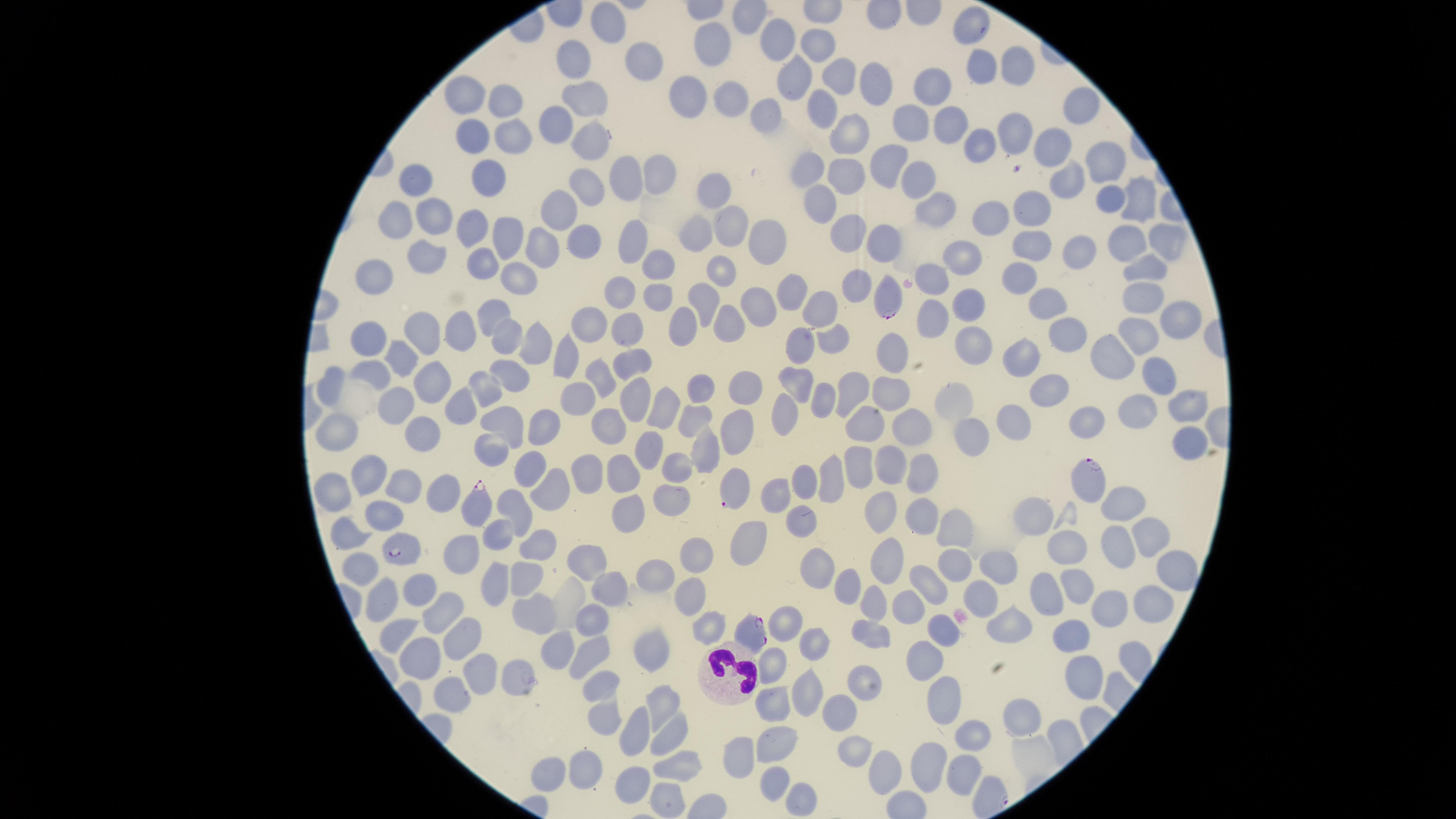 Approximate marker points as {x, y} in pixels. White blood cells: {721, 674}. Uninfected red blood cells: {605, 18}, {975, 27}, {782, 36}, {714, 42}, {818, 47}, {645, 57}, {568, 60}, {981, 65}, {1018, 66}, {796, 78}, {844, 78}, {873, 80}, {933, 87}, {691, 90}, {466, 95}, {586, 96}, {502, 100}, {734, 101}, {824, 106}, {1079, 113}, {764, 117}, {913, 120}, {556, 121}, {944, 125}, {1009, 133}, {469, 134}, {507, 137}, {850, 137}, {590, 139}, {973, 146}, {1049, 150}, {1102, 164}, {892, 166}, {665, 168}, {808, 168}, {629, 170}, {844, 172}, {485, 181}, {916, 181}, {589, 184}, {418, 185}, {1062, 185}, {708, 192}, {1133, 199}, {1110, 202}, {824, 204}, {927, 209}, {556, 212}, {1037, 212}, {436, 215}, {999, 216}, {397, 221}, {734, 224}, {475, 230}, {771, 233}, {1169, 233}, {502, 236}, {845, 236}, {583, 239}, {887, 239}, {692, 240}, {1123, 240}, {637, 241}, {1033, 246}, {538, 248}, {1079, 248}, {429, 255}, {963, 255}, {484, 260}, {664, 263}, {1145, 268}, {716, 272}, {378, 275}, {1018, 276}, {933, 279}, {518, 280}, {859, 282}, {617, 289}, {785, 289}, {704, 296}, {654, 297}, {760, 297}, {1141, 300}, {969, 301}, {1048, 304}, {825, 306}, {933, 312}, {492, 317}, {1176, 318}, {623, 324}, {589, 325}, {684, 329}, {732, 330}, {461, 332}, {370, 334}, {1141, 336}, {428, 337}, {1064, 338}, {505, 339}, {838, 339}, {533, 341}, {804, 346}, {980, 347}, {896, 348}, {564, 353}, {1111, 353}, {1029, 356}, {399, 357}, {626, 362}, {370, 369}, {1154, 369}, {507, 378}, {598, 380}, {332, 381}, {433, 382}, {701, 383}, {801, 383}, {740, 386}, {895, 387}, {1047, 387}, {852, 388}, {483, 394}, {825, 396}, {958, 399}, {577, 400}, {392, 404}, {630, 405}, {1175, 405}, {665, 406}, {786, 406}, {460, 408}, {1138, 410}, {693, 414}, {503, 418}, {1090, 419}, {1014, 422}, {611, 424}, {733, 424}, {541, 427}, {920, 427}, {423, 428}, {337, 429}, {970, 437}, {1190, 444}, {486, 447}, {703, 450}, {643, 451}, {889, 464}, {671, 467}, {859, 467}, {530, 470}, {922, 470}, {626, 472}, {367, 473}, {584, 473}, {827, 480}, {331, 486}, {803, 486}, {401, 487}, {445, 488}, {546, 491}, {667, 494}, {775, 495}, {1121, 501}, {628, 509}, {881, 510}, {516, 511}, {382, 512}, {804, 517}, {921, 517}, {501, 529}, {952, 530}, {1147, 531}, {348, 539}, {747, 540}, {537, 542}, {1111, 545}, {1067, 550}, {452, 551}, {887, 555}, {584, 558}, {694, 558}, {360, 566}, {815, 566}, {949, 566}, {997, 567}, {653, 574}, {496, 575}, {526, 577}, {1180, 580}, {932, 581}, {1073, 581}, {847, 583}, {422, 584}, {607, 586}, {981, 591}, {1048, 591}, {871, 592}, {689, 594}, {381, 598}, {902, 598}, {1153, 602}, {442, 604}, {534, 606}, {1107, 609}, {590, 617}, {788, 621}, {1008, 621}, {704, 624}, {871, 630}, {942, 631}, {397, 632}, {456, 637}, {1074, 637}, {817, 641}, {557, 642}, {651, 647}, {594, 649}, {421, 653}, {923, 656}, {773, 663}, {469, 668}, {1081, 673}, {510, 675}, {599, 684}, {863, 684}, {806, 692}, {951, 696}, {444, 701}, {661, 702}, {774, 703}, {834, 709}, {602, 717}, {1020, 717}, {637, 726}, {667, 729}, {972, 730}, {779, 740}, {853, 751}, {738, 755}, {921, 758}, {678, 764}, {585, 768}, {549, 771}, {954, 771}, {873, 775}, {771, 778}, {634, 779}, {669, 788}, {796, 797}. Parasitized red blood cells: {887, 297}, {1089, 478}, {730, 488}, {481, 509}, {407, 548}, {750, 631}. Circular visible region. Giemsa-stained preparation. Thin blood film. Species: Plasmodium falciparum. One field of view of the specimen. Presence: malaria parasites detected. Smartphone photograph through the microscope eyepiece. Image is 1456×819 pixels.